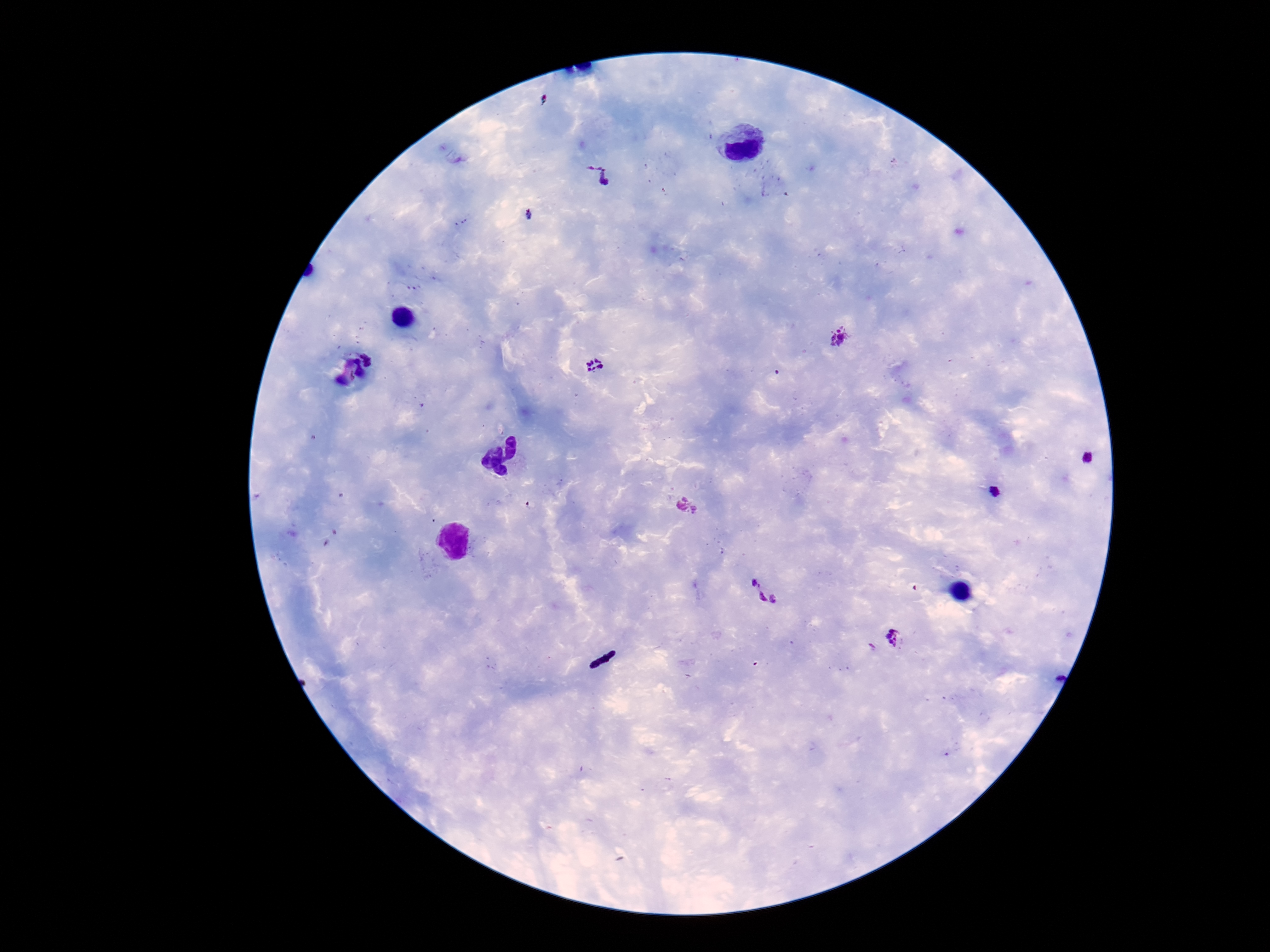

Plasmodium parasite locations = approximate object centers, in pixels from the top-left corner: (x=599, y=176), (x=528, y=215), (x=838, y=338), (x=594, y=364), (x=1087, y=459), (x=994, y=492), (x=687, y=505), (x=763, y=591), (x=895, y=637), (x=871, y=648)
patient malaria status = positive
preparation = thick peripheral-blood smear
magnification = 100x
image size = 1270×952 pixels
capture = smartphone camera through the microscope eyepiece
stain = Giemsa
field of view = single